Classify this cell by malaria status.
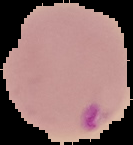
It is parasitized.

image type = segmented cell region with the area outside set to black
image size = 133×145 pixels
preparation = thin blood smear